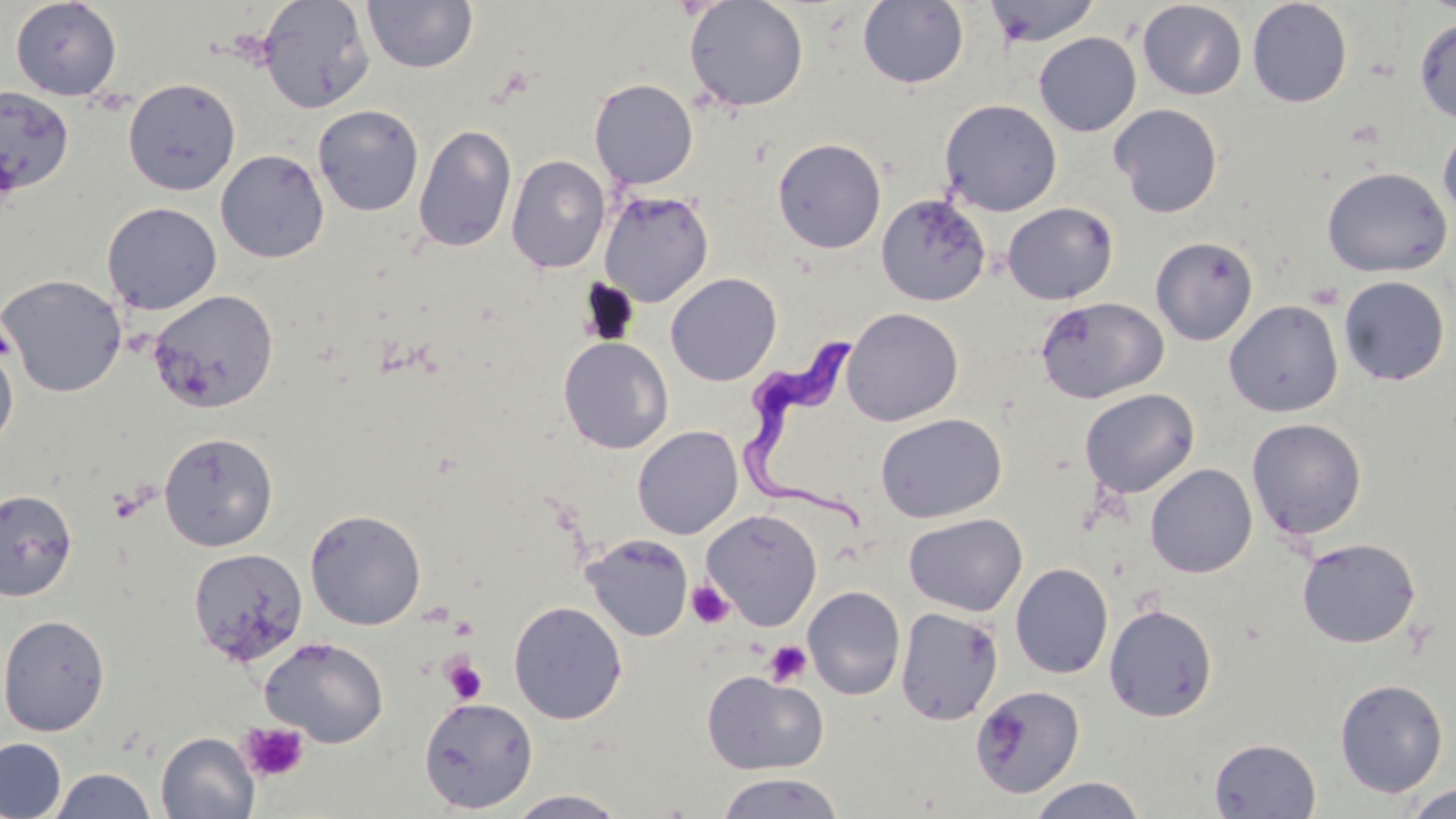

slide-level diagnosis = Trypanosoma brucei
preparation = thin blood smear
modality = light microscopy
image size = 1456×819 pixels
uninfected red blood cell locations = approximate bounding boxes as (x1,y1)-(x2,y2) corner pairs in pixels: (10,0)-(122,100), (257,0)-(375,113), (363,0)-(478,74), (684,0)-(809,112), (857,0)-(969,89), (983,0)-(1102,47), (1137,1)-(1247,100), (1247,1)-(1353,108), (1414,16)-(1456,124), (1033,32)-(1141,136), (123,78)-(241,195), (589,78)-(698,189), (0,85)-(75,198), (940,98)-(1062,216), (1109,103)-(1223,218), (312,104)-(424,216), (414,123)-(517,253), (1438,126)-(1456,226), (772,137)-(887,253), (215,149)-(329,263), (506,154)-(610,273), (1321,166)-(1452,277), (598,189)-(714,307), (876,193)-(991,306), (102,201)-(222,315), (1002,202)-(1118,304), (1150,236)-(1259,345), (665,272)-(782,386), (0,273)-(127,397), (1338,275)-(1451,386), (148,289)-(279,414), (1036,296)-(1168,403), (1224,299)-(1344,417), (842,307)-(963,425), (558,336)-(674,454), (0,340)-(18,453), (1079,388)-(1200,498), (875,413)-(1007,524), (1247,417)-(1367,540), (632,425)-(743,539), (158,432)-(278,551), (1145,463)-(1257,578), (0,488)-(78,602), (304,508)-(427,630), (701,509)-(823,630), (903,513)-(1027,616), (581,533)-(694,641), (1297,537)-(1421,648), (187,548)-(309,666), (1010,562)-(1113,679), (802,585)-(906,700), (508,600)-(628,724), (1104,604)-(1218,722), (895,607)-(1004,725), (0,614)-(110,736), (260,636)-(389,747), (702,670)-(827,775), (1334,678)-(1449,798), (971,685)-(1085,799), (418,696)-(538,813), (156,731)-(259,819), (0,737)-(67,818), (1209,738)-(1321,818), (48,767)-(158,819), (714,772)-(845,818), (1027,776)-(1148,818), (1403,783)-(1456,818), (504,789)-(631,819)
platelet locations = approximate bounding boxes as (x1,y1)-(x2,y2) corner pairs in pixels: (0,325)-(15,361), (685,581)-(735,629), (448,616)-(477,641), (764,640)-(813,687), (440,655)-(488,705), (238,721)-(309,783)
field of view = single
magnification = 1000x
Trypanosoma brucei locations = approximate bounding boxes as (x1,y1)-(x2,y2) corner pairs in pixels: (743,334)-(878,529)
stain = May-Grünwald-Giemsa